Report the malaria status of this cell.
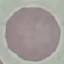

It is uninfected.

{
  "image_type": "automatically extracted cell patch, resized to 64 × 64 pixels",
  "capture": "smartphone camera at the microscope eyepiece",
  "stain": "Giemsa",
  "preparation": "thin blood smear"
}